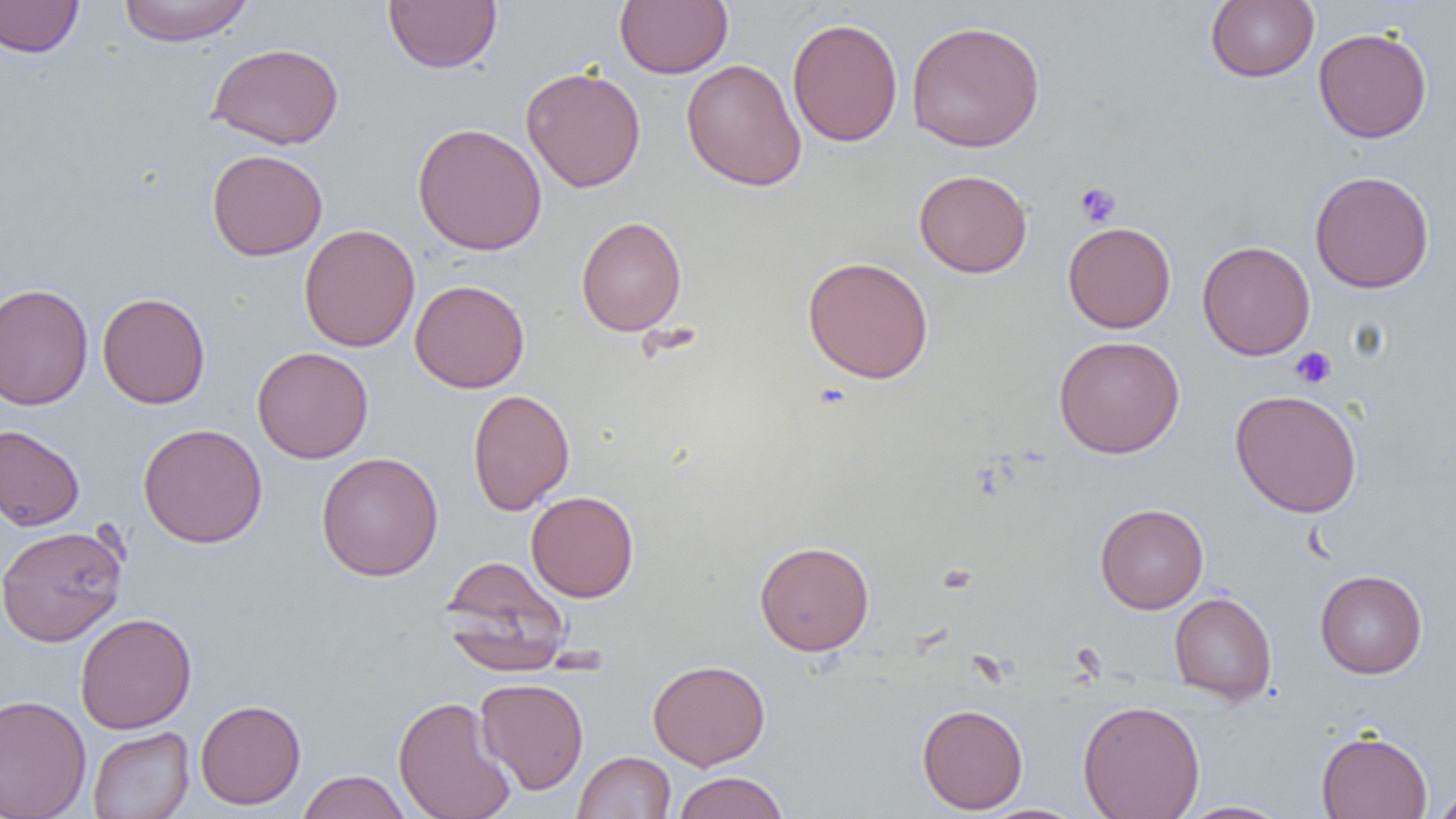
Summary:
  - Coordinate format: approximate bounding boxes as (x1,y1)-(x2,y2) corner pairs in pixels
  - Platelet locations: (1075,182)-(1121,228), (1290,346)-(1337,389)
  - Uninfected red blood cell locations: (117,0)-(255,46), (383,0)-(502,74), (615,0)-(733,78), (1205,0)-(1319,83), (0,1)-(84,58), (787,17)-(903,147), (905,20)-(1045,152), (1313,27)-(1432,143), (207,42)-(344,150), (681,58)-(806,192), (521,66)-(646,193), (412,122)-(547,256), (206,149)-(328,261), (914,169)-(1032,278), (1309,170)-(1435,293), (576,216)-(687,335), (1063,221)-(1176,333), (299,224)-(420,352), (1197,240)-(1316,361), (802,255)-(934,384), (410,279)-(530,393), (0,282)-(94,411), (97,292)-(210,409), (1053,335)-(1185,458), (252,346)-(373,463), (467,388)-(574,515), (1230,389)-(1362,518), (138,423)-(268,548), (0,425)-(85,531), (316,452)-(444,581), (526,490)-(639,602), (1095,503)-(1208,614), (0,525)-(127,647), (754,540)-(875,656), (441,556)-(571,673), (1314,569)-(1428,679), (1169,592)-(1277,705), (75,613)-(197,734), (647,659)-(771,770), (475,678)-(589,794), (0,694)-(92,819), (394,695)-(515,819), (195,698)-(306,810), (1078,699)-(1205,819), (916,703)-(1028,814), (88,726)-(194,819), (1315,729)-(1432,819), (573,751)-(676,818), (297,770)-(411,819), (672,771)-(789,819), (1430,788)-(1456,818), (1177,800)-(1291,818), (977,804)-(1088,819)
  - Slide-level diagnosis: negative for blood parasites
  - Preparation: thin blood smear
  - Magnification: 1000x
  - Image size: 1456×819 pixels
  - Field of view: single
  - Modality: light microscopy